Report the malaria status.
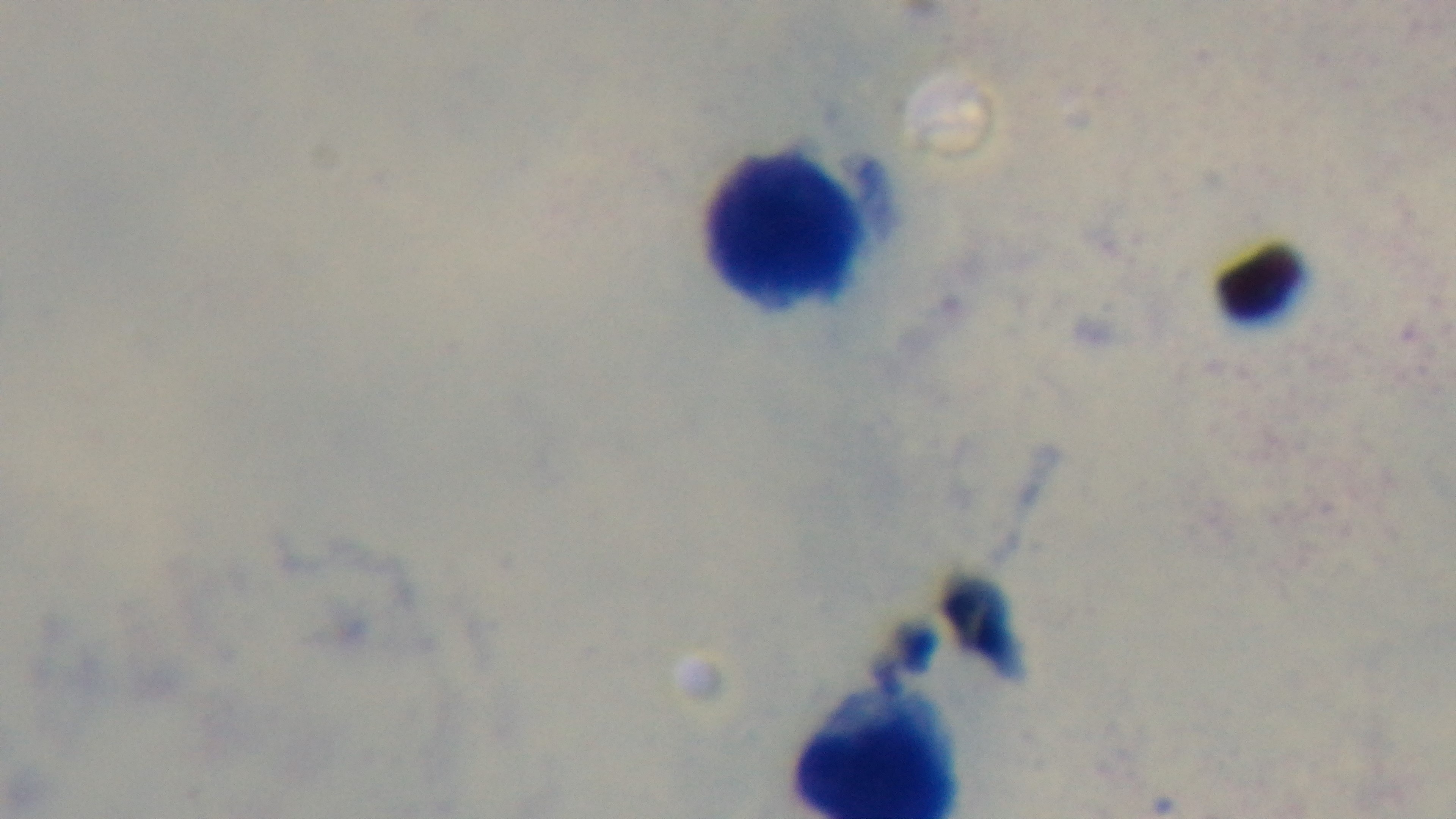

Uninfected.

capture = mounted 4K digital camera
objective = 100x oil immersion
preparation = thick smear
modality = light microscopy
field of view = one from the slide
stain = Giemsa